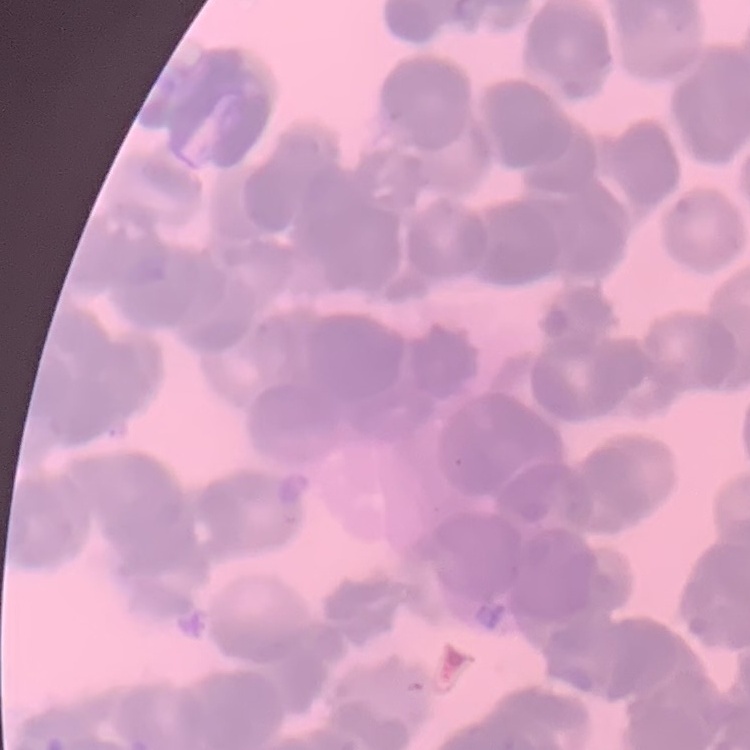

Summary:
  - Red blood cell morphology: rouleaux formation
  - Preparation: thin blood film
  - Stain: Field's or Giemsa
  - Image type: square crop of a larger photomicrograph